Report the malaria status of this cell.
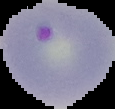
It is parasitized.

Summary:
  - Image type: segmented cell region on a black background
  - Image size: 115×109 pixels
  - Preparation: thin blood smear